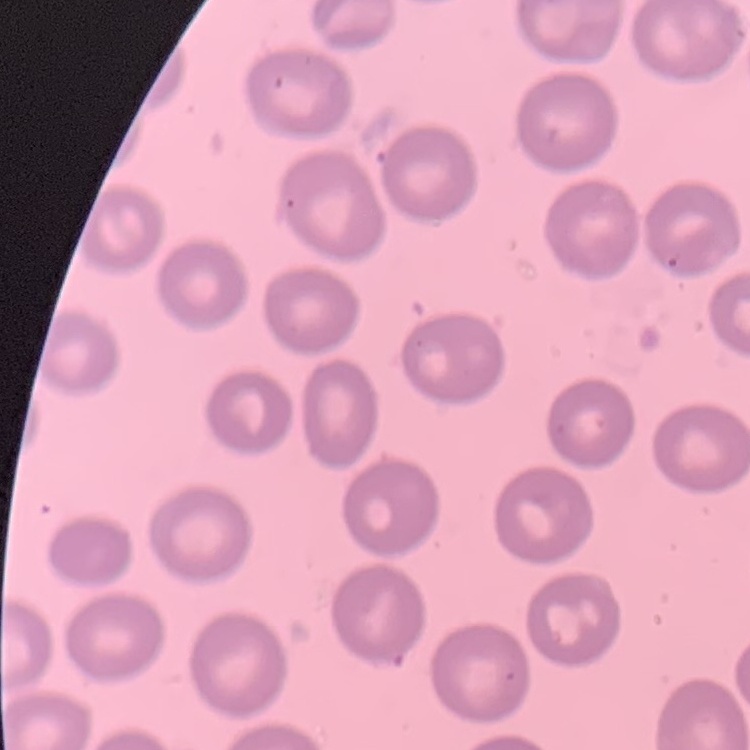 The red blood cells exhibit no rouleaux formation. One tile cut from a larger photomicrograph. Field's or Giemsa stain. Thin blood film.